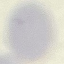
Summary:
  - Malaria status: uninfected
  - Stain: Giemsa
  - Preparation: thin smear
  - Capture: smartphone camera at the microscope eyepiece
  - Image type: cell patch, automatically extracted from a larger field of view and resized to 64 × 64 pixels